Locate and identify every blood parasite.
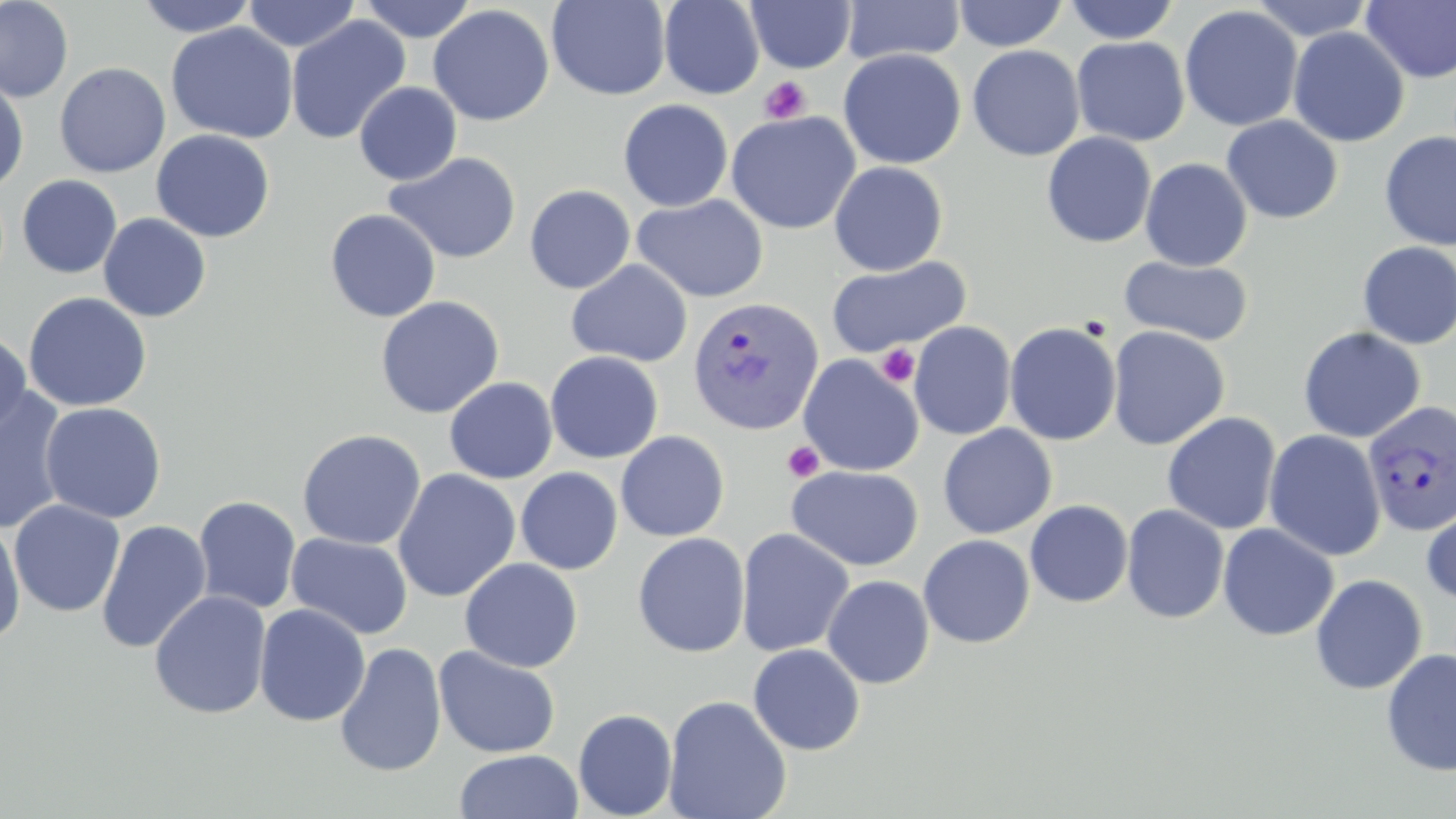
Approximate bounding boxes as (x1,y1)-(x2,y2) corner pairs in pixels.
Plasmodium vivax-infected red blood cells: (687,296)-(823,438), (1362,400)-(1456,537).
No Plasmodium falciparum, Plasmodium ovale, Plasmodium malariae, Babesia divergens, or Trypanosoma brucei observed.

{
  "slide_level_diagnosis": "Plasmodium vivax",
  "uninfected_red_blood_cell_locations": "approximate bounding boxes as (x1,y1)-(x2,y2) corner pairs in pixels: (0,0)-(74,103), (134,0)-(259,37), (243,0)-(361,52), (357,0)-(477,42), (546,0)-(671,101), (658,0)-(765,100), (1248,0)-(1376,41), (745,1)-(856,73), (841,1)-(965,65), (953,1)-(1069,51), (1063,1)-(1181,44), (1360,1)-(1456,83), (428,5)-(555,126), (1179,5)-(1303,132), (286,16)-(410,145), (165,22)-(299,143), (1287,27)-(1409,147), (1072,36)-(1190,146), (967,44)-(1085,161), (838,48)-(966,169), (54,62)-(171,178), (0,77)-(29,193), (354,81)-(462,185), (618,98)-(733,212), (725,111)-(861,235), (1221,115)-(1343,224), (151,129)-(276,242), (1379,131)-(1455,250), (1041,132)-(1156,248), (383,151)-(522,264), (1140,158)-(1253,271), (828,161)-(948,276), (17,174)-(122,278), (524,185)-(635,294), (632,194)-(768,302), (324,208)-(441,322), (98,213)-(211,322), (1356,241)-(1456,350), (1119,255)-(1254,346), (825,257)-(972,357), (566,259)-(693,367), (22,292)-(153,412), (375,295)-(504,419), (909,321)-(1016,440), (1004,322)-(1121,446), (1107,325)-(1229,450), (1297,327)-(1426,443), (0,331)-(31,436), (545,351)-(663,464), (798,355)-(924,477), (444,377)-(558,484), (0,387)-(71,535), (40,402)-(167,523), (1161,412)-(1282,535), (938,424)-(1057,539), (297,428)-(426,550), (1264,430)-(1386,561), (615,431)-(730,541), (786,465)-(924,571), (515,467)-(623,575), (392,468)-(521,602), (193,496)-(301,614), (1421,496)-(1456,608), (8,499)-(125,617), (1025,500)-(1133,608), (1121,504)-(1229,625), (0,519)-(26,647), (95,519)-(212,654), (1218,523)-(1340,641), (736,527)-(854,657), (632,532)-(750,658), (287,533)-(413,639), (918,535)-(1035,648), (459,558)-(584,673), (1310,573)-(1428,695), (822,575)-(935,688), (149,589)-(272,719), (254,603)-(371,727), (334,643)-(447,777), (748,643)-(865,755), (433,645)-(561,759), (1380,648)-(1456,777), (663,694)-(792,819), (573,708)-(677,819), (453,749)-(584,819)",
  "preparation": "thin blood smear",
  "magnification": "1000x",
  "platelet_locations": "approximate bounding boxes as (x1,y1)-(x2,y2) corner pairs in pixels: (758,76)-(811,125), (876,344)-(920,387), (782,440)-(824,483)",
  "modality": "light microscopy",
  "image_size": "1456×819 pixels",
  "field_of_view": "single",
  "stain": "May-Grünwald-Giemsa"
}